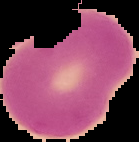 Image is 139×142 pixels. From a thin blood smear. Malaria status: uninfected. Segmented cell region on a black background.